Point out each malaria parasite and each leukocyte.
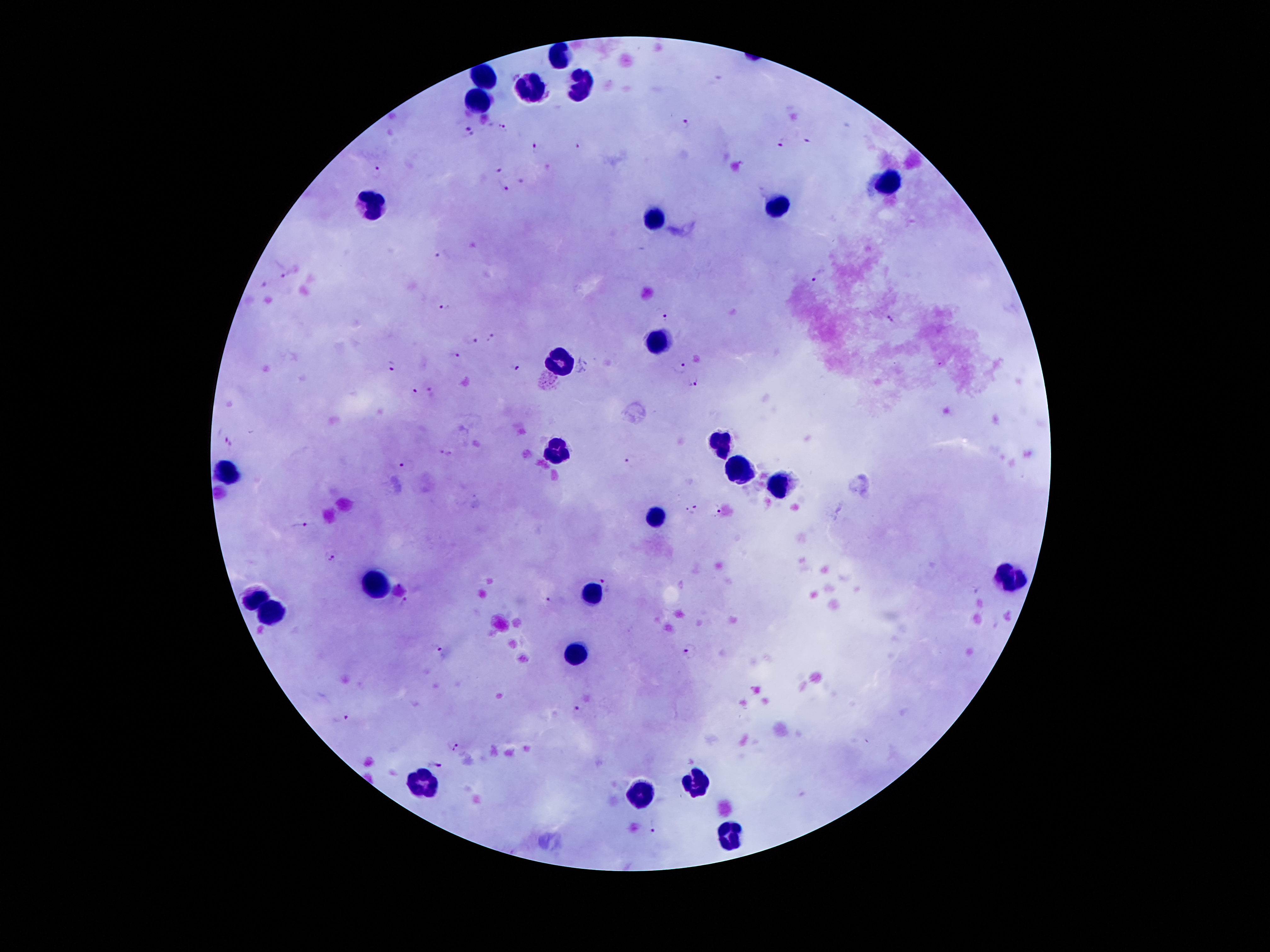

Approximate centers as [x, y] in pixels.
Malaria parasites: [687, 122], [463, 124], [501, 128], [472, 138], [809, 139], [783, 141], [577, 143], [537, 148], [376, 171], [497, 171], [520, 179], [505, 187], [443, 254], [289, 270], [817, 277], [266, 283], [446, 307], [665, 316], [889, 321], [493, 336], [470, 338], [453, 353], [941, 364], [390, 366], [515, 367], [682, 367], [695, 378], [415, 389], [431, 392], [228, 440], [447, 452], [630, 463], [406, 465], [717, 508], [689, 510], [301, 526], [330, 560], [608, 583], [976, 591], [549, 601], [405, 603], [437, 648], [688, 650], [579, 711], [341, 719], [452, 746], [435, 766], [653, 825].
Leukocytes: [559, 55], [486, 79], [582, 88], [532, 89], [480, 101], [886, 185], [373, 205], [779, 205], [655, 217], [657, 342], [563, 361], [718, 442], [555, 453], [741, 469], [226, 472], [777, 485], [658, 519], [1011, 579], [375, 585], [593, 593], [253, 597], [271, 613], [579, 652], [421, 783], [698, 783], [638, 794], [734, 835].

Summary:
  - Stain: Giemsa
  - Field of view: one from this slide
  - Preparation: thick blood film
  - Magnification: 100x
  - Patient malaria status: infected with Plasmodium falciparum
  - Image size: 1270×952 pixels
  - Capture: smartphone camera through the microscope eyepiece